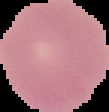

Image is 109×112 pixels. Segmented cell region on a black background. Malaria status: uninfected. From a thin blood smear.